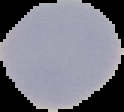
malaria_status: uninfected
image_size: 124×112 pixels
preparation: thin blood film
image_type: segmented cell region on a black background